State which parasite is depicted.
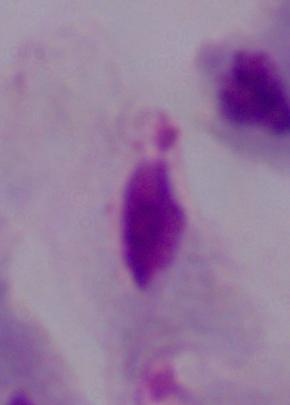

A trichomonad.

modality = photomicrograph
magnification = 1000x